Assess this cell for malaria.
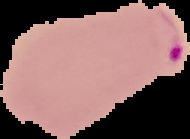

It is parasitized.

Summary:
  - Image type: segmented cell region on a black background
  - Image size: 190×139 pixels
  - Preparation: thin blood smear